Identify the cell.
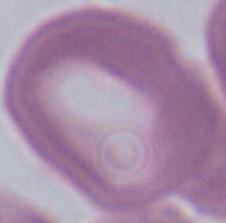
An erythrocyte.

magnification: 1000x
modality: micrograph